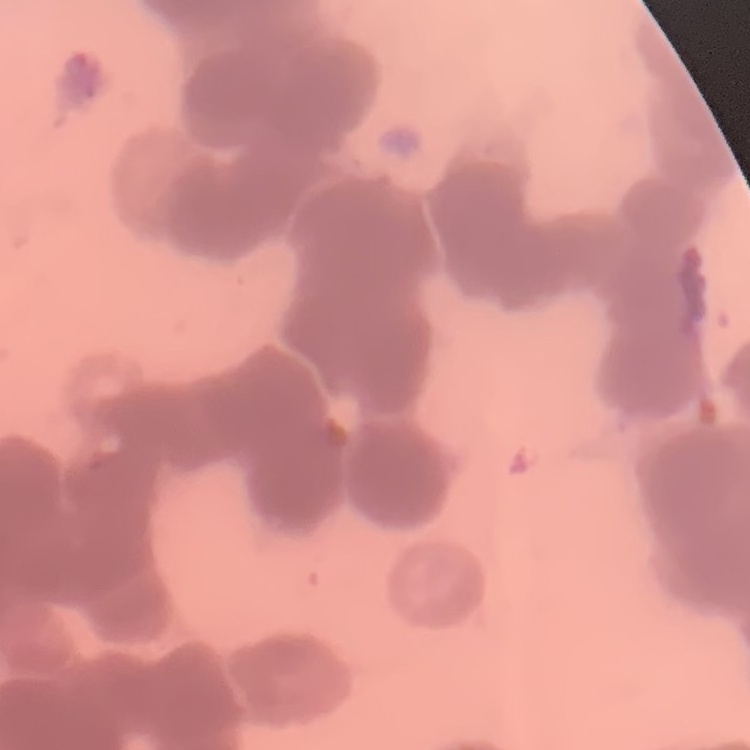

red blood cell morphology = rouleaux formation
preparation = thin peripheral smear
image type = square crop of a larger photomicrograph
stain = Field's or Giemsa